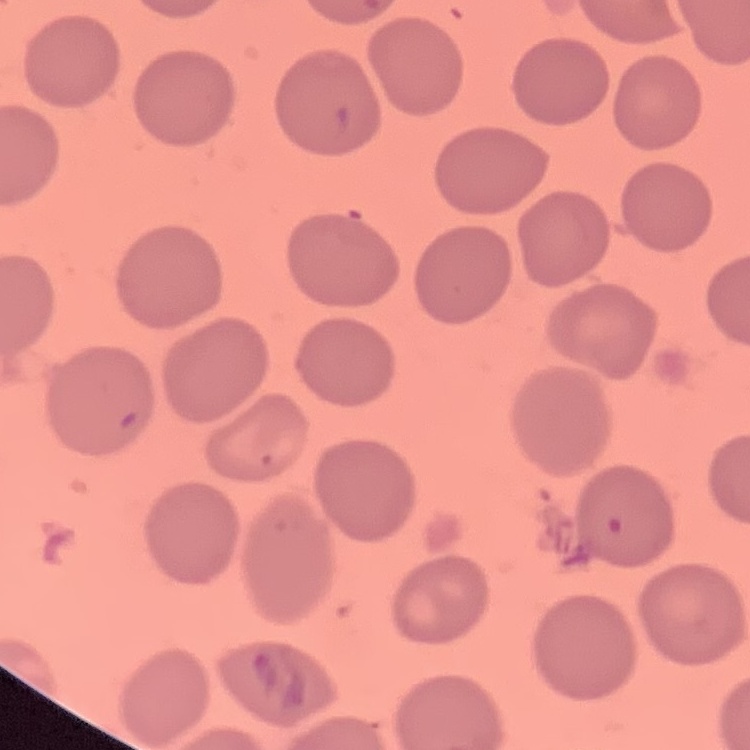

The erythrocytes exhibit no rouleaux formation. Thin blood smear. Stained with either Field's or Giemsa. Square crop of a larger photomicrograph.